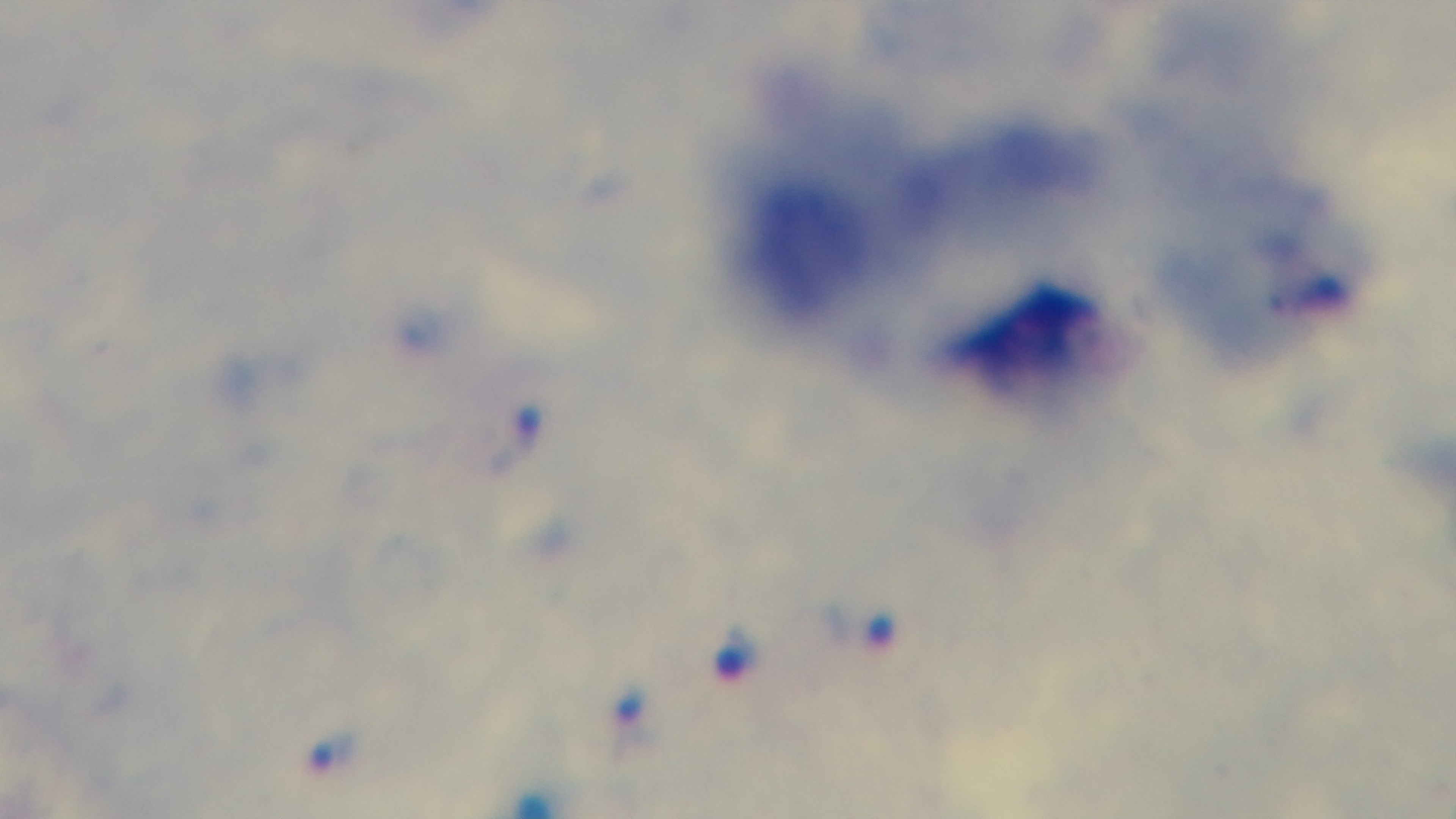
Giemsa stain. Oil-immersion objective, 100x. Captured with a mounted 4K digital camera. Photomicrograph. Malaria status: positive. One field from the slide. Preparation: thick.